Assess the morphology of the erythrocytes.
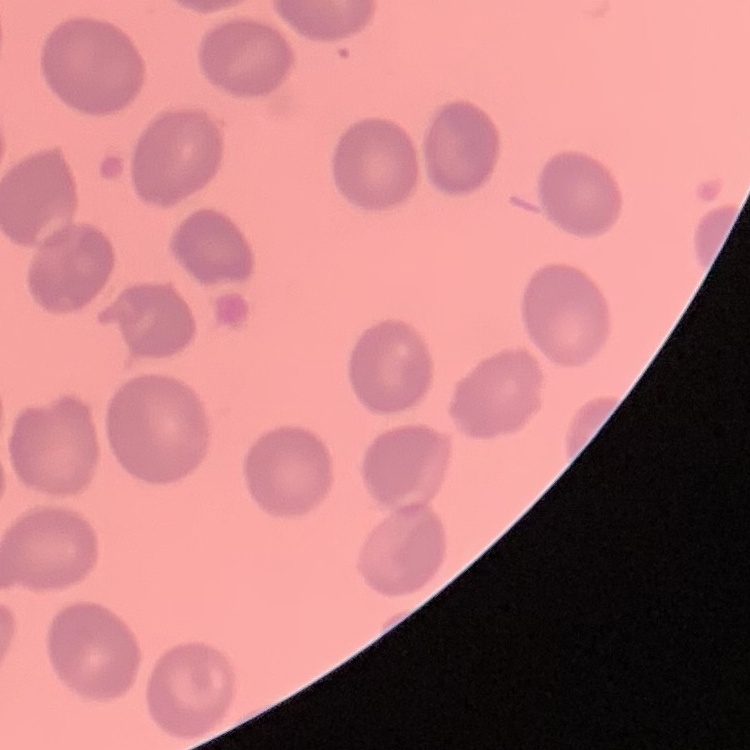

They show no rouleaux formation.

Summary:
  - Preparation: thin peripheral smear
  - Stain: Field's or Giemsa
  - Image type: square crop of a larger photomicrograph